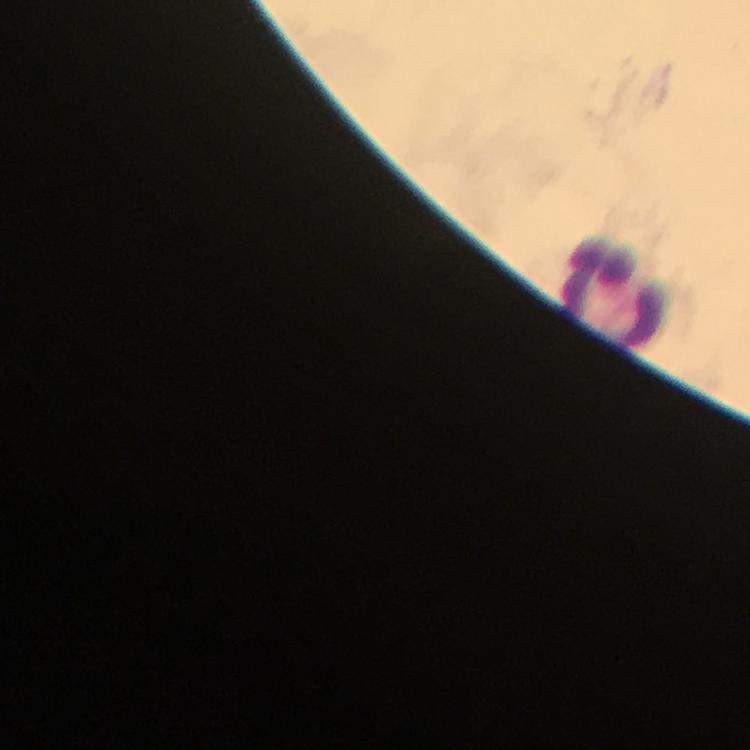 Approximate centers as {x, y} in pixels. Leukocyte locations: {613, 290}. Photographed through the microscope with a smartphone camera. Giemsa stain. Plasmodium parasites: none seen. Image is 750×750 pixels. 100x magnification. A crop from one field of view. Thick blood film. Immersion oil applied. From a diagnostic examination for malaria.